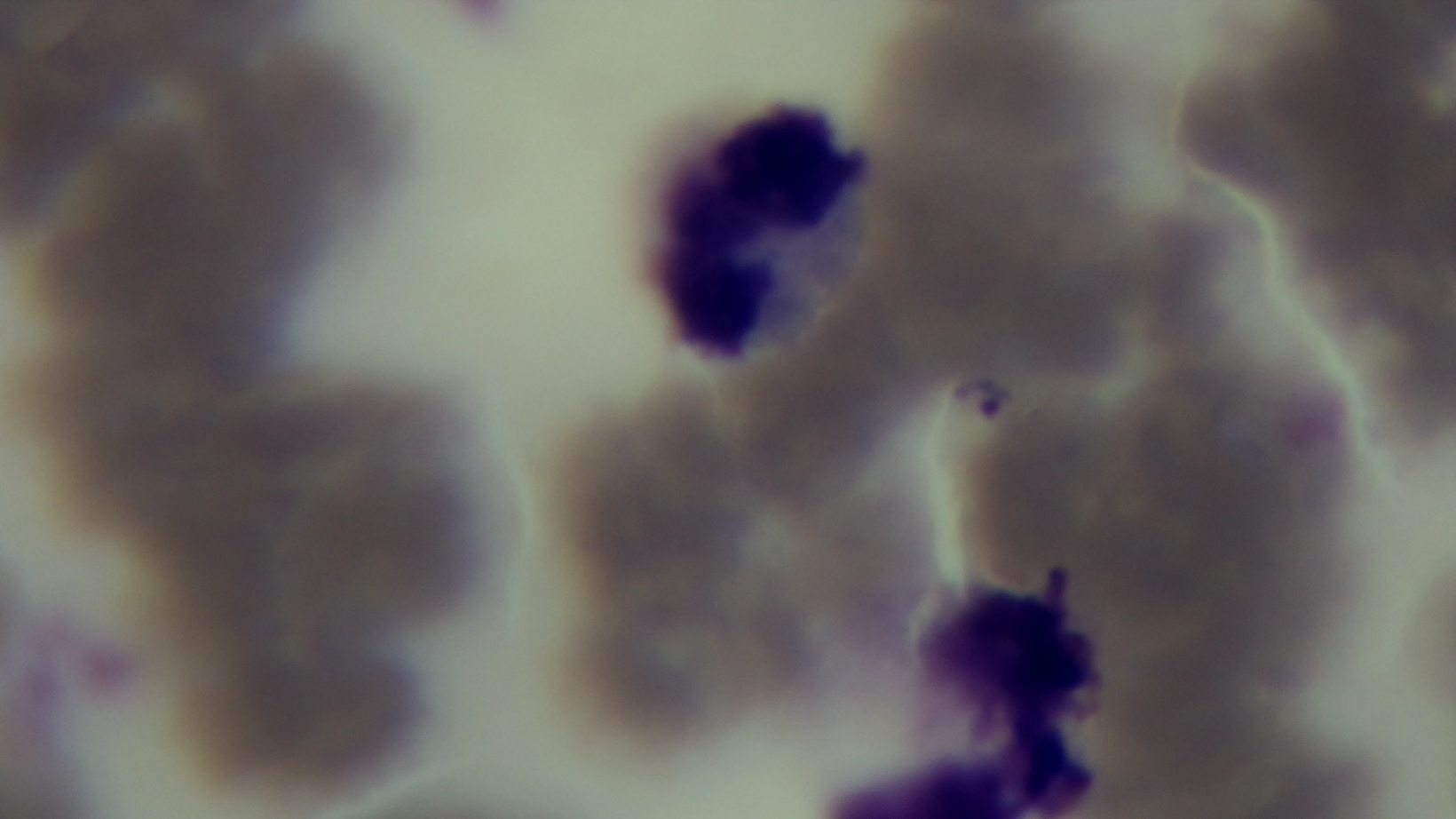 Mounted 4K digital camera. Giemsa-stained. Light microscopy. Oil-immersion objective, 100x. Preparation: thin smear. Malaria status: infected. One field from the slide.